Report the malaria status of this cell.
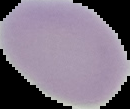
It is uninfected.

Summary:
  - Image type: segmented cell region on a black background
  - Preparation: thin blood smear
  - Image size: 130×109 pixels